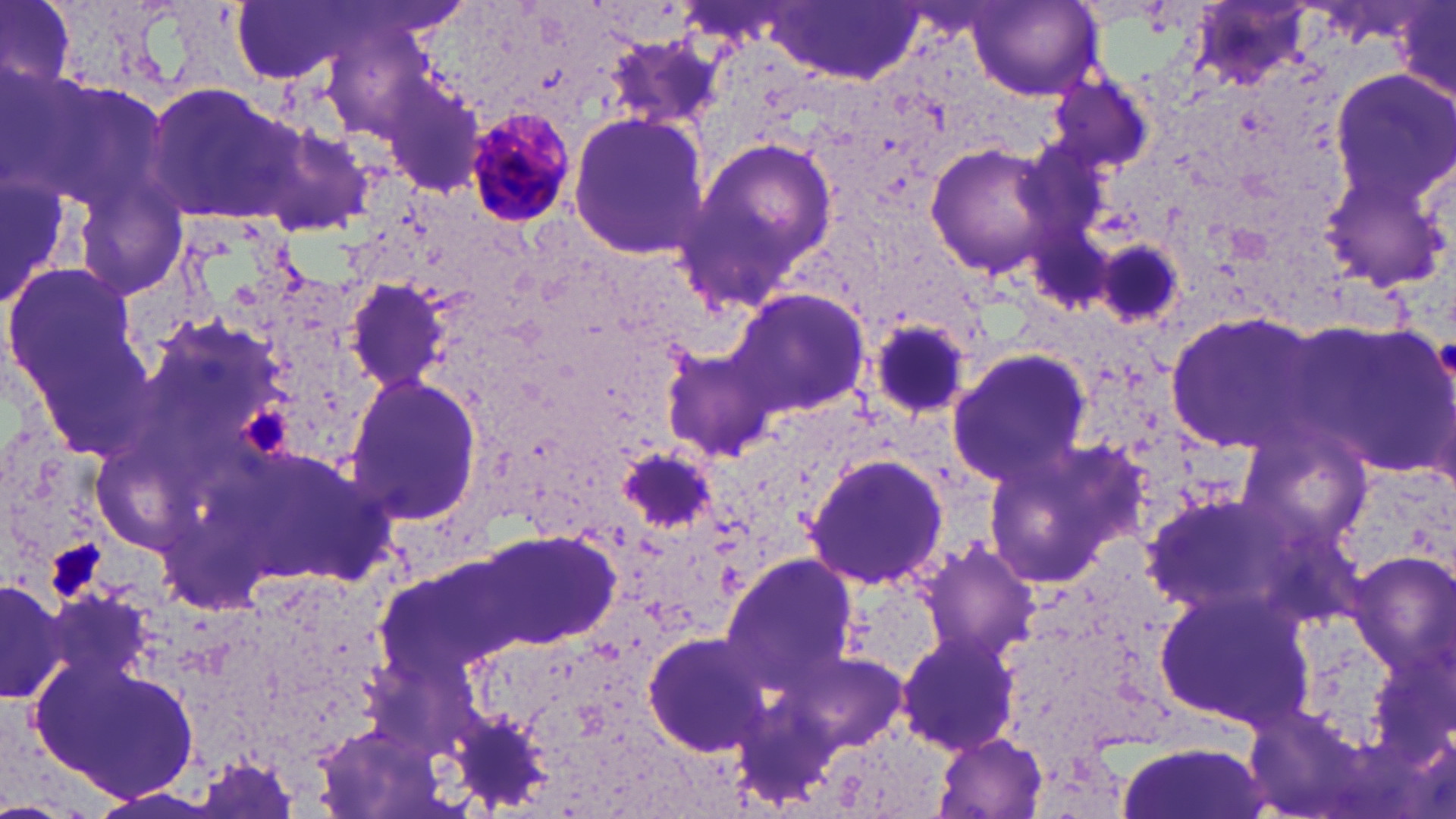
{
  "slide_level_diagnosis": "Plasmodium malariae",
  "modality": "optical microscopy",
  "preparation": "thin blood film",
  "uninfected_red_blood_cell_locations": "approximate bounding boxes as (x1, y1, x2, y2) in pixels: (1, 0, 76, 91), (226, 0, 386, 85), (968, 1, 1103, 102), (767, 2, 924, 87), (1392, 3, 1456, 108), (604, 33, 727, 139), (1328, 70, 1456, 211), (1049, 75, 1153, 172), (377, 80, 485, 198), (143, 83, 310, 225), (566, 114, 708, 257), (245, 120, 382, 239), (1320, 133, 1454, 289), (680, 136, 841, 306), (923, 142, 1064, 281), (1088, 234, 1189, 331), (2, 255, 157, 461), (344, 279, 451, 390), (728, 287, 872, 420), (1164, 311, 1329, 457), (863, 318, 977, 423), (1292, 320, 1456, 477), (946, 348, 1093, 489), (662, 350, 773, 462), (342, 371, 483, 526), (1236, 429, 1376, 555), (976, 445, 1139, 588), (618, 447, 717, 536), (805, 452, 951, 590), (1138, 492, 1298, 622), (479, 531, 619, 649), (918, 540, 1040, 661), (1353, 548, 1456, 685), (723, 553, 855, 687), (0, 573, 71, 706), (1153, 585, 1309, 727), (896, 629, 1020, 755), (642, 632, 772, 755), (29, 653, 201, 806), (933, 732, 1044, 816), (1117, 736, 1269, 819)",
  "platelet_locations": "approximate bounding boxes as (x1, y1, x2, y2) in pixels: (244, 409, 291, 456), (48, 544, 108, 596)",
  "field_of_view": "one of a larger specimen",
  "image_size": "1456×819 pixels",
  "stain": "May-Grünwald-Giemsa",
  "magnification": "1000x",
  "plasmodium_malariae_infected_red_blood_cell_locations": "approximate bounding boxes as (x1, y1, x2, y2) in pixels: (460, 107, 577, 228)"
}